Identify the parasite.
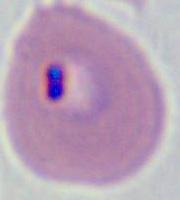
Plasmodium.

Micrograph. 400x or 1000x magnification.